Name the cell type shown.
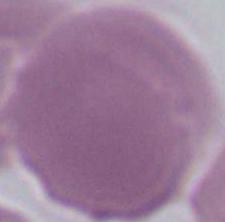

An erythrocyte.

Photomicrograph. 1000x magnification.